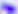
modality = photomicrograph
magnification = 400x
identification = Toxoplasma gondii